State the preparation type.
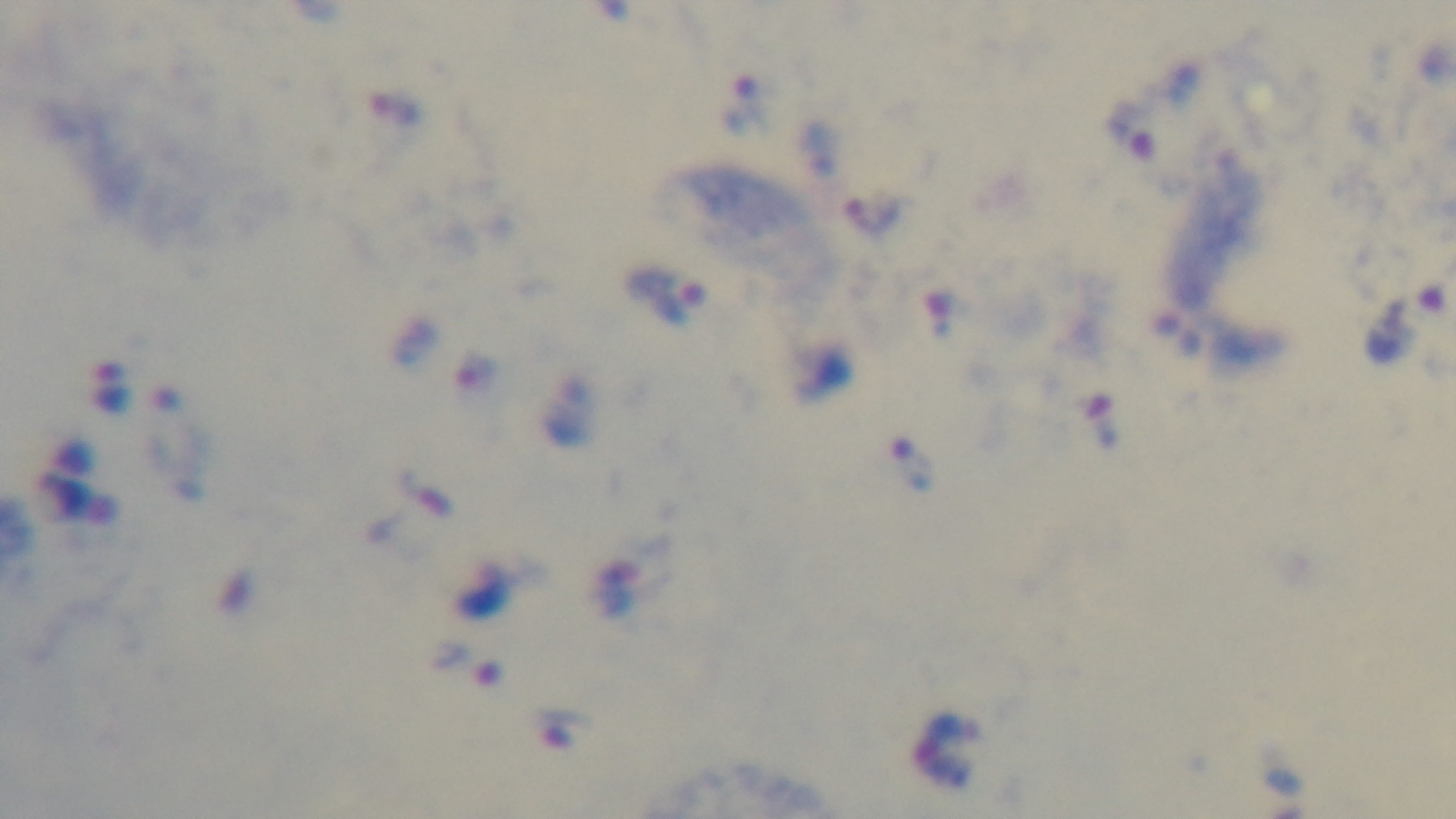
Thick.

Summary:
  - Malaria status: infected
  - Field of view: one from the slide
  - Objective: 100x oil immersion
  - Capture: mounted 4K digital camera
  - Stain: Giemsa
  - Modality: light microscopy